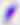
{
  "identification": "Toxoplasma gondii",
  "modality": "photomicrograph",
  "magnification": "400x"
}